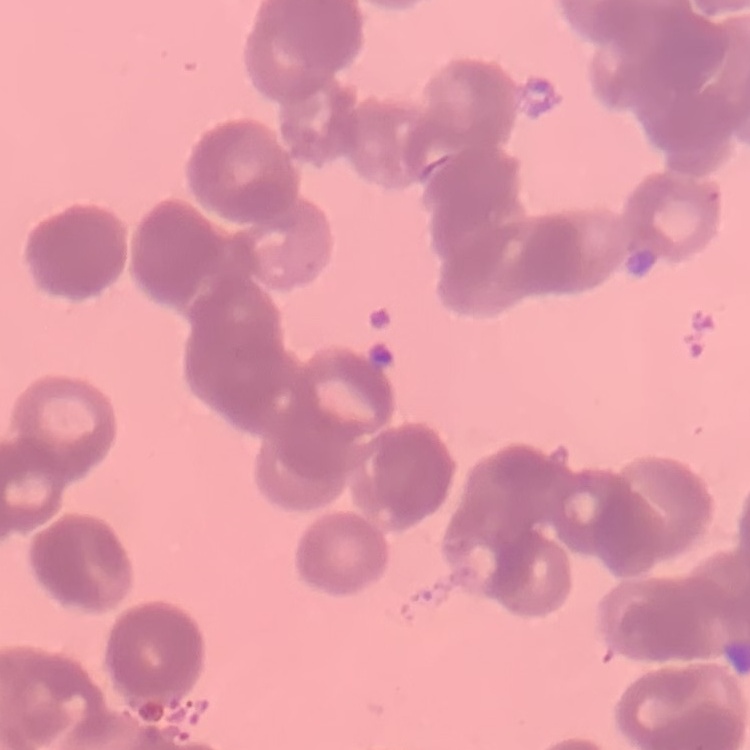
Summary:
  - Erythrocyte morphology: rouleaux formation
  - Stain: Field's or Giemsa
  - Image type: square crop of a larger photomicrograph
  - Preparation: thin blood smear